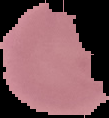
Result: negative for Plasmodium parasites. Segmented cell region on a black background. Image is 109×118 pixels. From a thin blood film.